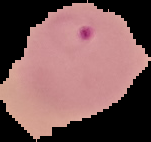 Segmented cell region on a black background. Image is 151×142 pixels. Result: malaria parasites identified. From a thin blood film.